Locate and identify every blood parasite.
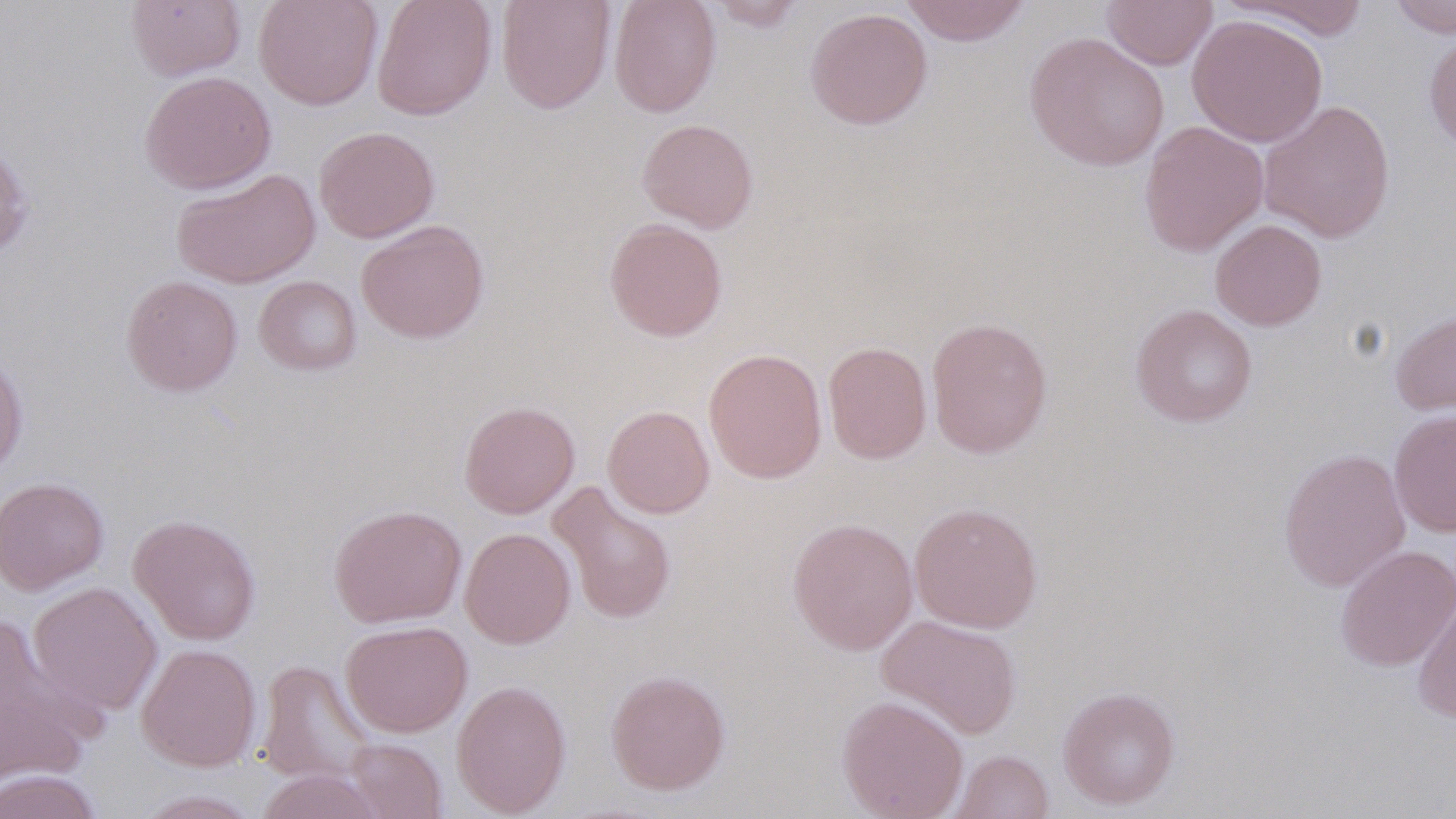

No blood parasites seen.

Approximate bounding boxes as (x1, y1, x2, y2) in pixels. Uninfected red blood cell locations: (126, 0, 246, 82), (253, 0, 383, 111), (372, 0, 497, 120), (496, 0, 615, 113), (609, 0, 721, 117), (707, 0, 806, 33), (899, 0, 1032, 46), (1102, 0, 1218, 69), (1389, 0, 1455, 38), (1221, 1, 1372, 40), (805, 7, 932, 130), (1187, 13, 1328, 147), (1423, 28, 1456, 154), (1024, 31, 1170, 172), (139, 70, 277, 194), (1258, 99, 1396, 243), (636, 118, 759, 233), (1139, 120, 1269, 257), (313, 126, 439, 243), (0, 142, 35, 259), (171, 168, 320, 288), (604, 217, 728, 342), (356, 219, 490, 344), (1210, 219, 1327, 330), (120, 275, 243, 396), (253, 275, 362, 376), (1130, 304, 1257, 427), (1389, 307, 1456, 417), (925, 316, 1052, 458), (822, 341, 932, 463), (703, 348, 827, 483), (0, 352, 28, 478), (459, 400, 580, 518), (602, 405, 714, 518), (1388, 409, 1456, 537), (1278, 448, 1411, 591), (0, 477, 109, 594), (548, 482, 677, 625), (909, 502, 1043, 633), (329, 504, 467, 628), (128, 514, 262, 645), (787, 516, 918, 655), (460, 527, 576, 649), (1335, 544, 1456, 672), (27, 581, 162, 718), (1412, 594, 1456, 723), (876, 614, 1021, 739), (340, 620, 472, 737), (0, 624, 99, 788), (136, 644, 261, 771), (256, 660, 377, 788), (605, 669, 730, 795), (452, 679, 572, 817), (1057, 686, 1180, 809), (836, 695, 969, 819), (342, 737, 447, 819), (949, 749, 1054, 819), (254, 768, 387, 819), (0, 769, 104, 818), (132, 789, 264, 818). Slide-level diagnosis: negative for blood parasites. Thin blood smear. One field of a larger specimen. Image is 1456×819 pixels. Light microscopy. May-Grünwald-Giemsa stain. Captured at 1000x magnification.